State the blood parasite species.
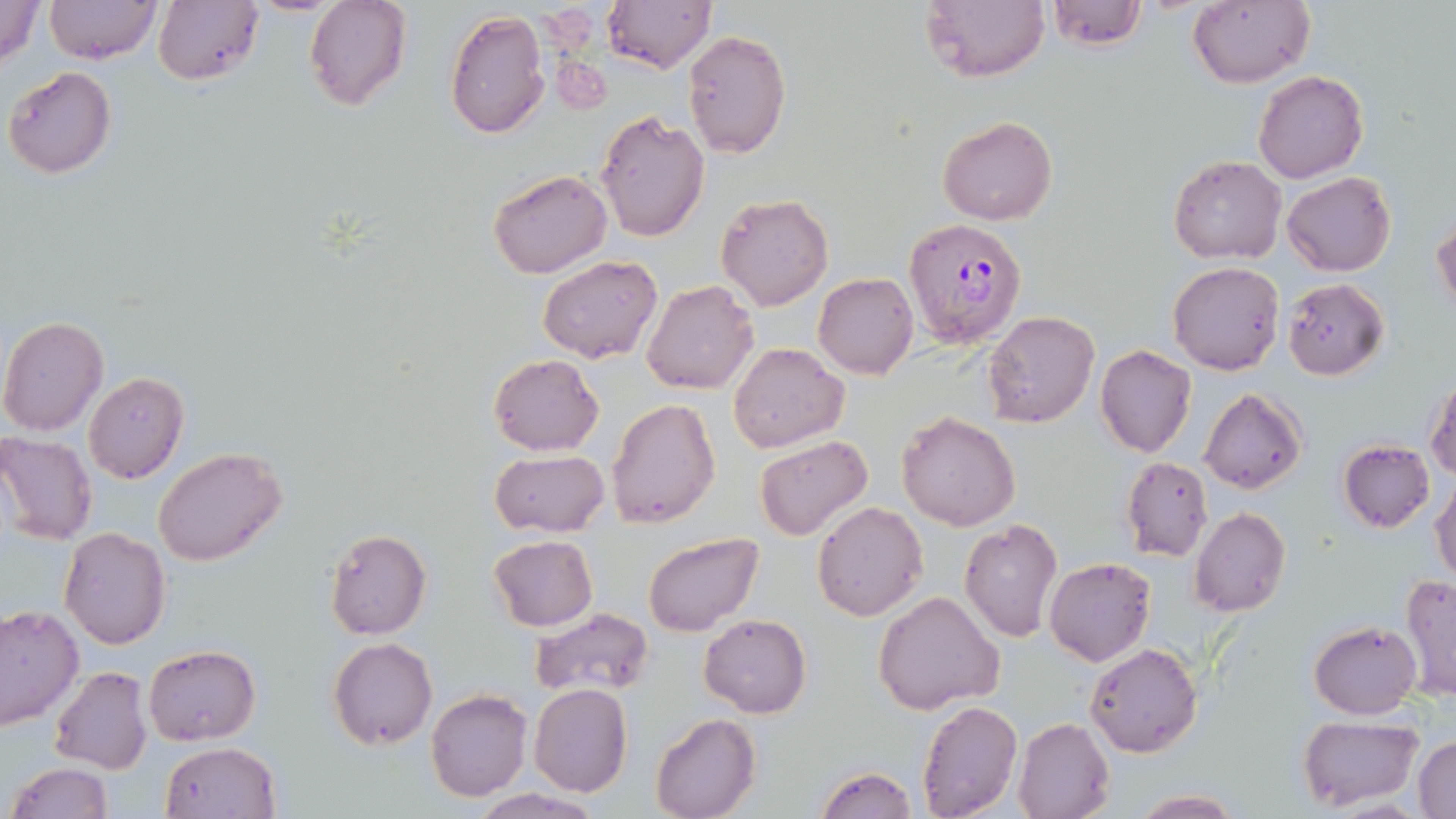

Plasmodium falciparum.

field of view = one of a larger specimen
stain = May-Grünwald-Giemsa
image size = 1456×819 pixels
preparation = thin blood smear
uninfected red blood cell locations = approximate bounding boxes as [x1, y1, x2, y2] in pixels: [0, 0, 47, 68], [44, 0, 162, 66], [153, 0, 264, 87], [304, 0, 411, 111], [602, 0, 715, 73], [1187, 0, 1313, 89], [921, 1, 1049, 84], [1045, 1, 1146, 51], [445, 8, 550, 140], [681, 30, 791, 157], [3, 66, 117, 179], [1253, 70, 1368, 184], [595, 111, 710, 242], [937, 116, 1058, 224], [1167, 155, 1286, 265], [487, 169, 612, 278], [1282, 172, 1395, 276], [715, 193, 834, 310], [1431, 217, 1456, 314], [538, 255, 663, 365], [1168, 261, 1284, 376], [812, 273, 918, 379], [1283, 278, 1388, 380], [642, 280, 759, 396], [983, 310, 1100, 429], [0, 317, 108, 436], [729, 341, 848, 454], [1095, 345, 1198, 458], [488, 354, 603, 455], [83, 371, 188, 485], [1426, 374, 1456, 482], [1199, 389, 1306, 493], [607, 397, 722, 528], [895, 411, 1020, 532], [0, 432, 97, 546], [754, 433, 874, 541], [1338, 439, 1434, 532], [154, 448, 288, 568], [490, 449, 609, 536], [1120, 457, 1213, 561], [1431, 477, 1456, 585], [811, 500, 929, 621], [1190, 507, 1290, 616], [958, 517, 1063, 642], [60, 527, 170, 647], [324, 529, 431, 640], [643, 533, 762, 636], [488, 535, 597, 630], [1044, 557, 1156, 667], [1400, 574, 1456, 701], [873, 592, 1005, 714], [0, 605, 83, 729], [528, 608, 654, 697], [699, 614, 812, 718], [1309, 620, 1422, 719], [327, 638, 438, 751], [1085, 642, 1202, 757], [143, 645, 261, 746], [48, 666, 152, 776], [529, 683, 633, 796], [426, 689, 531, 802], [917, 701, 1022, 818], [650, 713, 760, 819], [1298, 715, 1421, 810], [1013, 717, 1115, 819], [1413, 736, 1456, 818], [158, 742, 280, 819], [7, 762, 112, 819], [815, 765, 918, 818], [1129, 789, 1243, 818], [471, 790, 601, 819]
modality = light microscopy
magnification = 1000x
Plasmodium falciparum-infected red blood cell locations = approximate bounding boxes as [x1, y1, x2, y2] in pixels: [906, 216, 1026, 346]